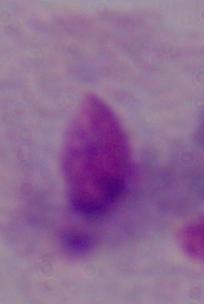
Summary:
  - Modality: micrograph
  - Identification: trichomonad
  - Magnification: 1000x